Name the parasite shown.
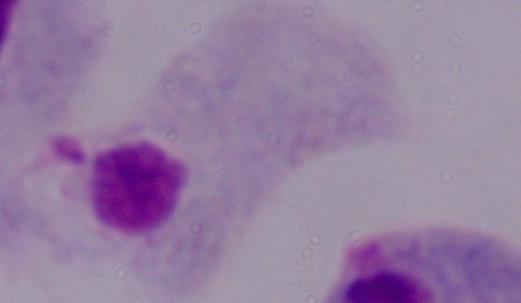

This is a trichomonad.

magnification = 1000x
modality = photomicrograph